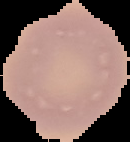

preparation = thin blood film
image type = cell region segmented out of the field of view; surrounding area masked to black
image size = 130×142 pixels
malaria status = uninfected